Locate every malaria parasite.
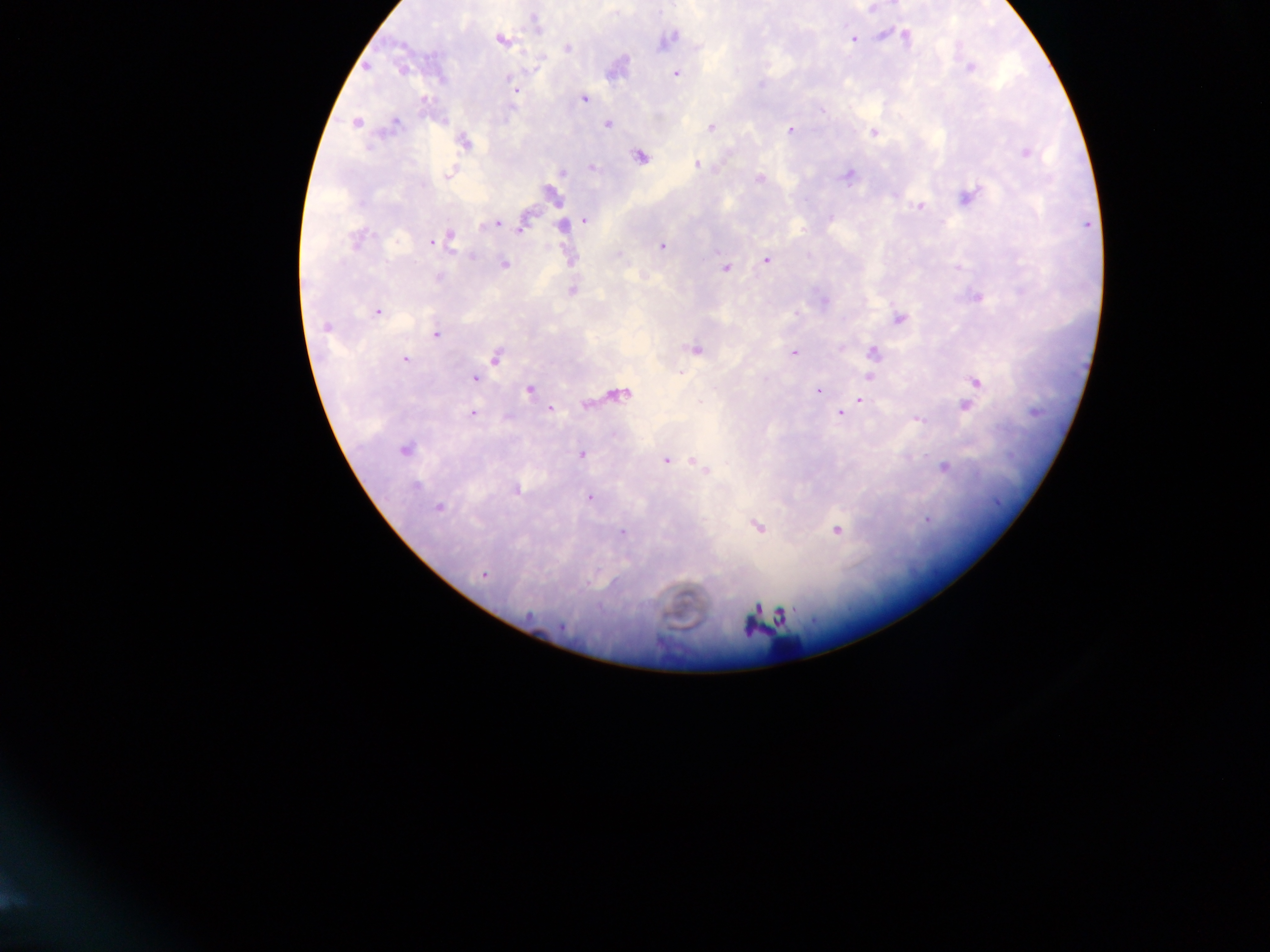
Approximate centers as {x, y} in pixels.
Malaria parasites: {871, 9}, {536, 24}, {884, 36}, {905, 36}, {668, 39}, {853, 39}, {500, 40}, {568, 48}, {367, 67}, {970, 68}, {402, 69}, {676, 74}, {513, 84}, {515, 91}, {583, 98}, {822, 111}, {356, 122}, {395, 124}, {608, 124}, {711, 127}, {790, 130}, {874, 132}, {464, 143}, {1026, 153}, {640, 157}, {698, 165}, {592, 168}, {561, 173}, {448, 175}, {847, 176}, {760, 178}, {553, 195}, {968, 196}, {920, 206}, {585, 220}, {497, 223}, {562, 226}, {523, 227}, {450, 236}, {439, 239}, {355, 241}, {432, 242}, {662, 246}, {766, 260}, {504, 264}, {726, 268}, {437, 277}, {572, 291}, {978, 298}, {378, 311}, {900, 319}, {326, 326}, {435, 334}, {695, 350}, {794, 353}, {873, 353}, {496, 357}, {405, 358}, {870, 377}, {474, 378}, {976, 382}, {529, 390}, {818, 390}, {620, 394}, {860, 400}, {586, 405}, {965, 405}, {551, 410}, {473, 413}, {839, 413}, {919, 421}, {405, 450}, {582, 454}, {666, 460}, {702, 467}, {944, 468}, {416, 485}, {517, 490}, {590, 497}, {439, 507}, {757, 527}, {837, 531}, {622, 532}, {484, 575}, {756, 608}, {782, 615}, {751, 623}.

Leukocyte locations (subset; some below the resolvable size): {784, 647}. Thick blood film. Single field of view. Mobile-phone photograph taken through the microscope. Image is 1270×952 pixels. Collected in Ghana.